Outline each blood parasite and name the species.
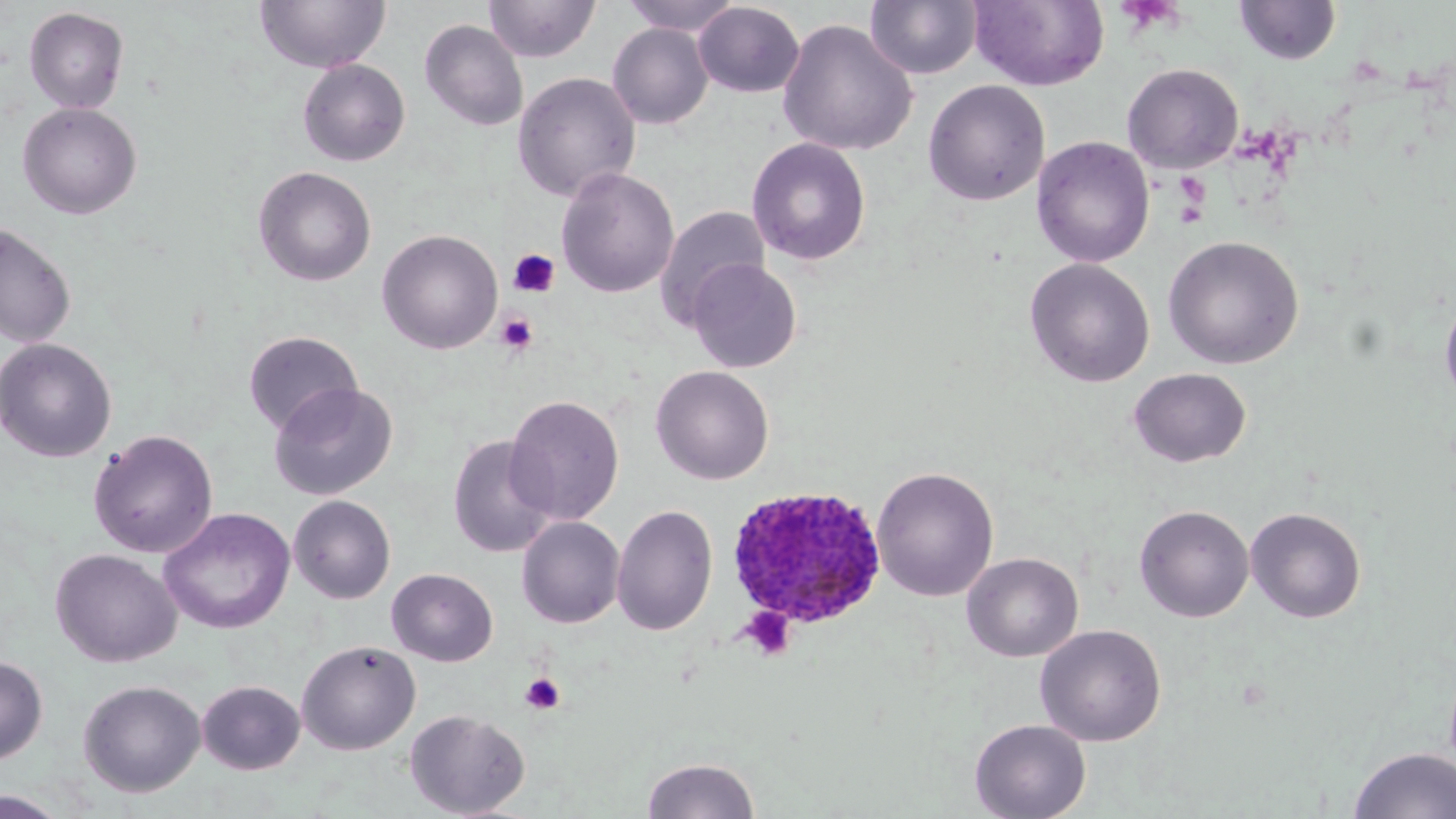

Approximate bounding boxes as [x1, y1, x2, y2] in pixels.
Plasmodium ovale-infected red blood cells: [726, 485, 887, 632].
No Plasmodium falciparum, Plasmodium malariae, Plasmodium vivax, Babesia divergens, or Trypanosoma brucei observed.

Platelet locations: [509, 249, 562, 298], [495, 311, 539, 355], [739, 606, 797, 662], [520, 672, 566, 715]. Uninfected red blood cell locations: [255, 0, 390, 74], [483, 0, 600, 63], [621, 0, 743, 36], [865, 0, 982, 80], [969, 0, 1110, 92], [1234, 1, 1341, 65], [693, 2, 804, 97], [23, 6, 129, 113], [777, 18, 918, 157], [419, 19, 529, 131], [608, 23, 713, 129], [298, 59, 410, 167], [1122, 63, 1244, 174], [512, 71, 641, 203], [923, 79, 1050, 206], [17, 102, 142, 219], [1032, 136, 1155, 268], [746, 137, 871, 266], [253, 166, 377, 286], [556, 167, 679, 298], [655, 205, 770, 327], [0, 223, 77, 349], [377, 229, 503, 354], [1163, 235, 1304, 369], [1023, 257, 1156, 387], [687, 258, 802, 373], [1439, 291, 1456, 408], [243, 330, 363, 435], [1, 338, 117, 463], [650, 364, 774, 485], [1128, 367, 1252, 468], [268, 381, 398, 501], [504, 394, 624, 525], [88, 429, 219, 559], [447, 434, 557, 558], [871, 466, 999, 601], [289, 495, 396, 604], [611, 504, 718, 636], [1134, 504, 1254, 622], [1245, 506, 1367, 623], [159, 508, 296, 634], [516, 516, 625, 629], [50, 548, 181, 667], [962, 552, 1083, 662], [387, 568, 498, 666], [1035, 624, 1167, 746], [296, 639, 420, 755], [0, 655, 48, 765], [78, 679, 206, 797], [196, 680, 305, 774], [404, 708, 531, 818], [969, 718, 1091, 819], [1349, 746, 1456, 819], [641, 756, 761, 818], [0, 790, 71, 818]. Slide-level diagnosis: Plasmodium ovale. Single field of view. Optical microscopy. Thin blood film. Image is 1456×819 pixels. Captured at 1000x magnification. May-Grünwald-Giemsa stain.